Assess this cell for malaria.
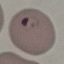
It is parasitized.

Thin blood film. Giemsa-stained preparation. Automatically extracted cell patch, resized to 64 × 64 pixels. Photographed with a smartphone camera at the microscope eyepiece.